Assess this cell for malaria.
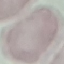

It is uninfected.

stain = Giemsa
preparation = thin blood film
image type = cell patch, automatically extracted from a larger field of view and resized to 64 × 64 pixels
capture = smartphone through the microscope eyepiece